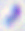

magnification = 400x
identification = Toxoplasma gondii
modality = micrograph